Identify the cell.
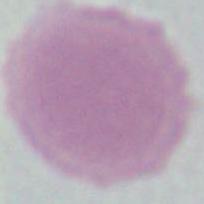

An erythrocyte.

magnification = 1000x
modality = photomicrograph